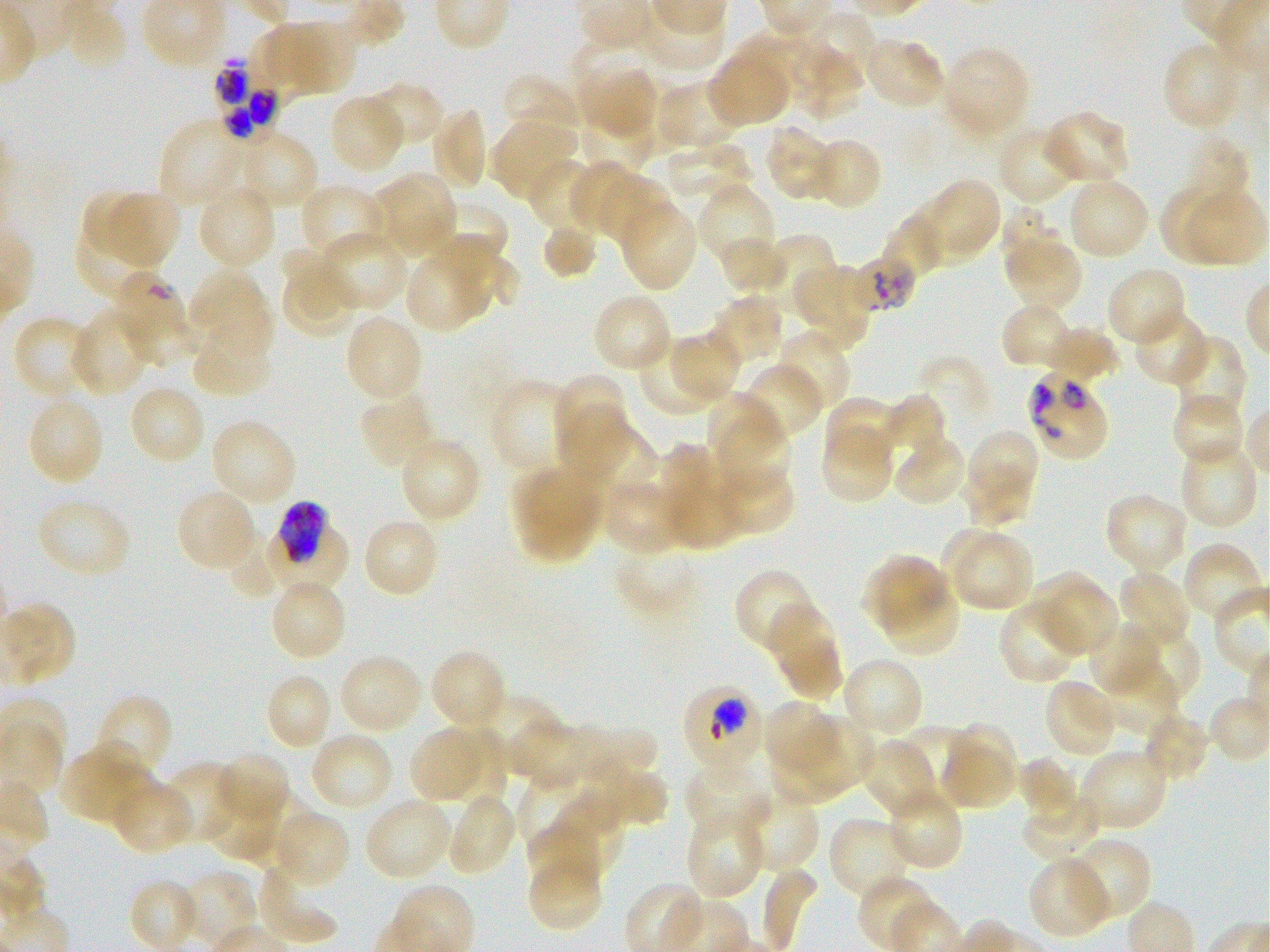

Approximate bounding boxes as (x1, y1, x2, y2) in pixels. Not every red blood cell is marked. A life-cycle stage — or a range of stages, where the recorded stages span more than one — follows each staged infected red blood cell.
Summary:
  - Locations of red blood cells of indeterminate infection status: (852, 246, 919, 318), (112, 272, 188, 341)
  - Locations of uninfected red blood cells: (63, 6, 126, 70), (804, 6, 886, 79), (266, 20, 355, 92), (572, 35, 656, 97), (862, 37, 947, 111), (1162, 39, 1242, 132), (795, 47, 866, 121), (945, 48, 1027, 136), (708, 57, 788, 128), (578, 61, 660, 142), (502, 73, 583, 152), (656, 80, 743, 154), (363, 81, 445, 149), (329, 94, 406, 175), (573, 95, 658, 178), (428, 108, 488, 193), (1040, 110, 1131, 188), (490, 117, 577, 202), (159, 121, 243, 203), (764, 124, 838, 202), (997, 126, 1075, 206), (233, 129, 319, 212), (1163, 134, 1251, 228), (814, 139, 879, 208), (666, 144, 761, 202), (525, 156, 600, 232), (570, 162, 631, 234), (367, 170, 458, 261), (601, 172, 672, 247), (1066, 176, 1150, 261), (929, 178, 1000, 255), (697, 180, 777, 270), (299, 183, 386, 262), (1157, 183, 1238, 259), (83, 184, 154, 262), (196, 184, 277, 272), (1185, 184, 1265, 265), (102, 190, 181, 268), (617, 197, 698, 292), (904, 199, 980, 265), (430, 203, 508, 267), (995, 203, 1062, 277), (73, 208, 165, 304), (881, 219, 949, 283), (541, 221, 596, 279), (436, 230, 522, 318), (317, 231, 407, 312), (766, 234, 837, 314), (717, 236, 792, 296), (1003, 242, 1080, 315), (279, 250, 356, 339), (406, 255, 481, 332), (790, 261, 879, 353), (1105, 266, 1187, 348), (187, 268, 273, 362), (591, 294, 673, 374), (711, 294, 784, 358), (1001, 302, 1077, 370), (125, 305, 199, 366), (70, 306, 153, 397), (1132, 309, 1211, 388), (343, 313, 423, 404), (12, 315, 99, 402), (1039, 327, 1119, 384), (192, 328, 274, 400), (775, 330, 851, 415), (673, 332, 737, 399), (1169, 336, 1246, 423), (641, 339, 713, 414), (915, 346, 995, 421), (738, 363, 824, 445), (552, 374, 629, 470), (488, 380, 574, 473), (128, 383, 207, 465), (359, 390, 437, 472), (1171, 392, 1245, 468), (26, 395, 105, 488), (708, 395, 786, 489), (879, 395, 946, 468), (823, 398, 899, 466), (560, 414, 655, 506), (209, 418, 298, 508), (819, 421, 896, 505), (961, 428, 1037, 489), (891, 434, 967, 509), (398, 435, 481, 524), (1179, 438, 1258, 529), (657, 447, 744, 552), (713, 460, 797, 538), (511, 463, 606, 563), (958, 470, 1030, 527), (602, 477, 689, 556), (175, 488, 258, 573), (1103, 491, 1189, 575), (35, 495, 132, 580), (361, 517, 440, 599), (939, 525, 1012, 600), (228, 531, 283, 596), (954, 536, 1031, 608), (615, 538, 702, 612), (1182, 542, 1265, 624), (859, 552, 952, 633), (734, 568, 819, 657), (1025, 570, 1107, 640), (1117, 570, 1192, 649), (269, 579, 347, 663), (885, 585, 958, 654), (1045, 586, 1119, 659), (999, 597, 1084, 687), (766, 601, 843, 699), (0, 602, 76, 687), (1086, 621, 1164, 698), (1122, 626, 1201, 705), (429, 648, 507, 732), (337, 653, 424, 737), (840, 656, 925, 740), (1090, 658, 1183, 743), (265, 673, 334, 752), (1044, 678, 1121, 758), (94, 693, 172, 781), (1207, 695, 1270, 763), (467, 696, 564, 775), (763, 700, 838, 769), (1142, 710, 1209, 782), (437, 718, 512, 816), (581, 718, 660, 785), (793, 718, 876, 792), (948, 720, 1018, 781), (515, 722, 598, 797), (410, 723, 487, 806), (899, 727, 980, 798), (308, 732, 395, 812), (860, 737, 939, 819), (767, 740, 852, 803), (62, 741, 152, 829), (939, 744, 1017, 807), (1077, 747, 1169, 832), (214, 753, 291, 831), (1018, 755, 1080, 823), (598, 756, 665, 826), (160, 762, 240, 845), (683, 762, 770, 840), (516, 773, 584, 842), (108, 776, 195, 855), (202, 781, 285, 864), (734, 785, 819, 871), (885, 785, 964, 871), (446, 791, 518, 877), (1021, 791, 1103, 862), (250, 792, 308, 867), (540, 792, 628, 875), (363, 796, 454, 882), (270, 808, 350, 890), (684, 809, 766, 901), (829, 817, 908, 897), (528, 822, 606, 887), (1060, 838, 1150, 926), (1028, 856, 1113, 939), (530, 858, 601, 927), (753, 859, 823, 952), (256, 861, 341, 946), (179, 870, 259, 947), (858, 876, 938, 949)
  - Locations of infected red blood cells: (213, 57, 284, 138); (1024, 368, 1109, 461); (265, 503, 350, 596) late trophozoite to early schizont; (682, 685, 762, 763)
  - Stain: Giemsa
  - Preparation: thin blood film
  - Culture: Plasmodium falciparum strain 3D7, static, in vitro
  - Donor blood group: O+
  - Field of view: one from this slide
  - Image size: 1270×952 pixels
  - Objective: 100x, oil immersion, numerical aperture 1.25